Outline each blood parasite and name the species.
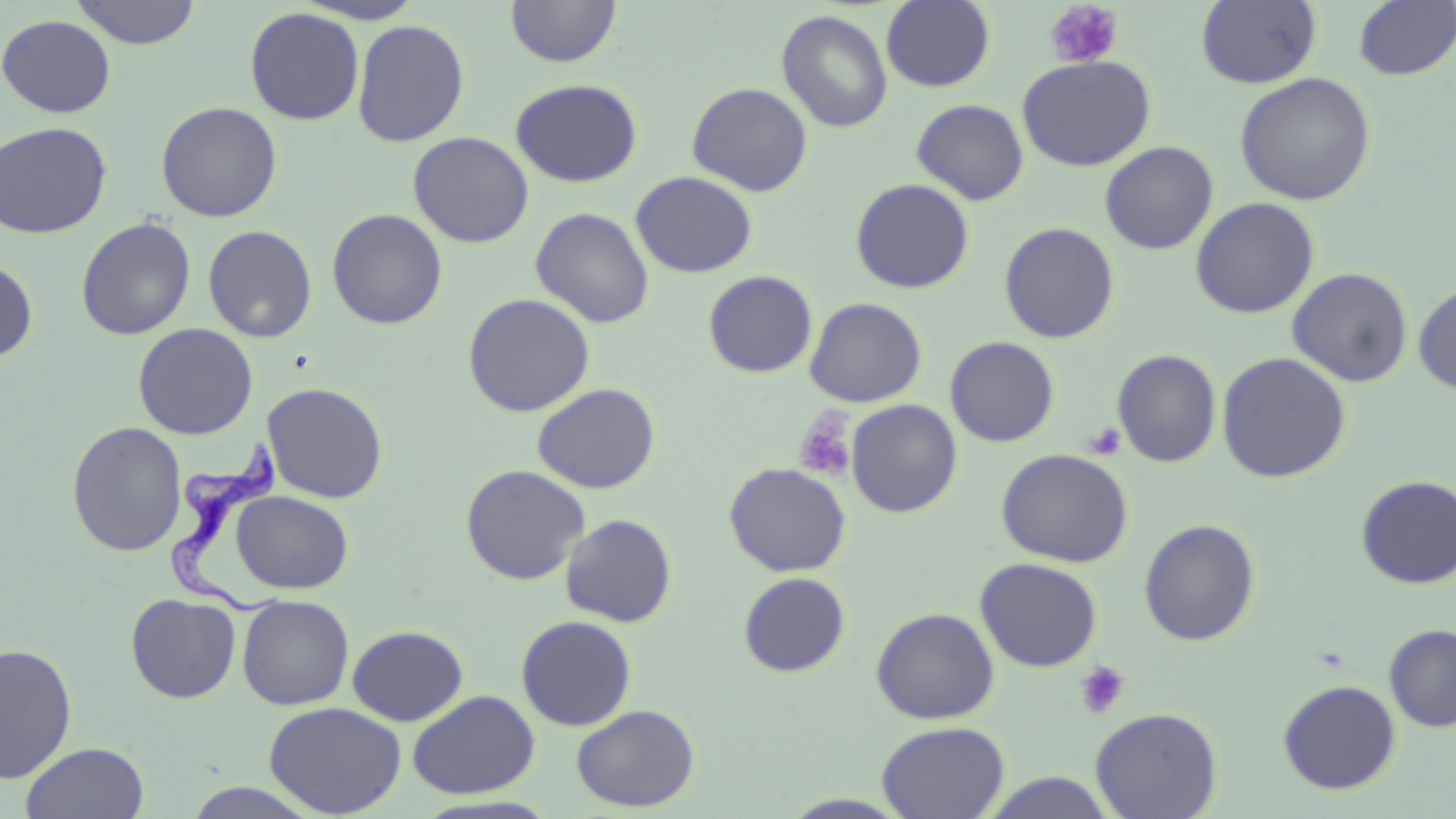
Approximate bounding boxes as (x1,y1)-(x2,y2) corner pairs in pixels.
Trypanosoma brucei: (151,432)-(293,620).
No Plasmodium falciparum, Plasmodium ovale, Plasmodium malariae, Plasmodium vivax, or Babesia divergens observed.

Uninfected red blood cell locations: (295,0)-(427,24), (1196,0)-(1323,88), (70,1)-(202,49), (505,1)-(622,68), (881,1)-(995,91), (1353,1)-(1455,81), (244,6)-(365,125), (776,9)-(893,133), (0,14)-(116,119), (352,19)-(470,147), (1017,55)-(1155,171), (1234,72)-(1376,206), (510,78)-(643,187), (687,82)-(813,196), (911,98)-(1029,204), (156,100)-(282,222), (0,121)-(113,239), (408,131)-(534,248), (1100,141)-(1218,255), (630,171)-(757,278), (850,178)-(975,294), (1190,197)-(1319,319), (530,206)-(655,329), (326,208)-(448,330), (76,217)-(196,340), (202,221)-(447,338), (999,222)-(1119,343), (202,224)-(317,343), (0,258)-(38,363), (1287,267)-(1413,387), (703,270)-(817,378), (1413,282)-(1456,395), (462,293)-(596,417), (804,297)-(927,407), (133,323)-(258,439), (945,336)-(1060,447), (1112,349)-(1222,468), (1216,352)-(1351,483), (262,382)-(389,503), (532,382)-(661,494), (846,399)-(963,517), (66,421)-(187,557), (996,448)-(1134,567), (724,463)-(851,577), (460,464)-(590,585), (1355,475)-(1456,588), (231,490)-(353,594), (560,513)-(678,627), (1138,518)-(1261,646), (975,557)-(1102,672), (738,572)-(851,678), (125,593)-(241,703), (237,595)-(354,710), (871,607)-(999,724), (516,615)-(637,731), (346,624)-(468,726), (1384,624)-(1456,732), (0,642)-(78,783), (1277,679)-(1401,795), (407,690)-(540,799), (263,701)-(406,817), (571,704)-(700,812), (1090,707)-(1223,819), (876,721)-(1010,819), (20,741)-(150,819), (982,771)-(1116,818), (180,782)-(326,818). Platelet locations: (1044,1)-(1123,69), (793,408)-(858,483), (1083,422)-(1126,460), (1074,660)-(1130,720). Slide-level diagnosis: Trypanosoma brucei. Optical microscopy. Thin blood film. May-Grünwald-Giemsa stain. Image is 1456×819 pixels. One field of a larger specimen. Captured at 1000x magnification.